Report the malaria status of this cell.
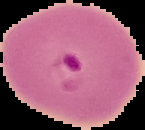
Parasitized.

image size = 145×130 pixels
preparation = thin blood film
image type = segmented cell region with the area outside set to black